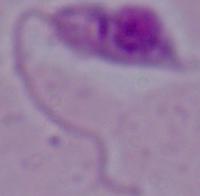
1000x magnification. Photomicrograph. A Leishmania parasite is shown.